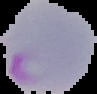

image type = cell region segmented out of the field of view; surrounding area masked to black
malaria status = parasitized
image size = 97×94 pixels
preparation = thin blood film